Identify the preparation type.
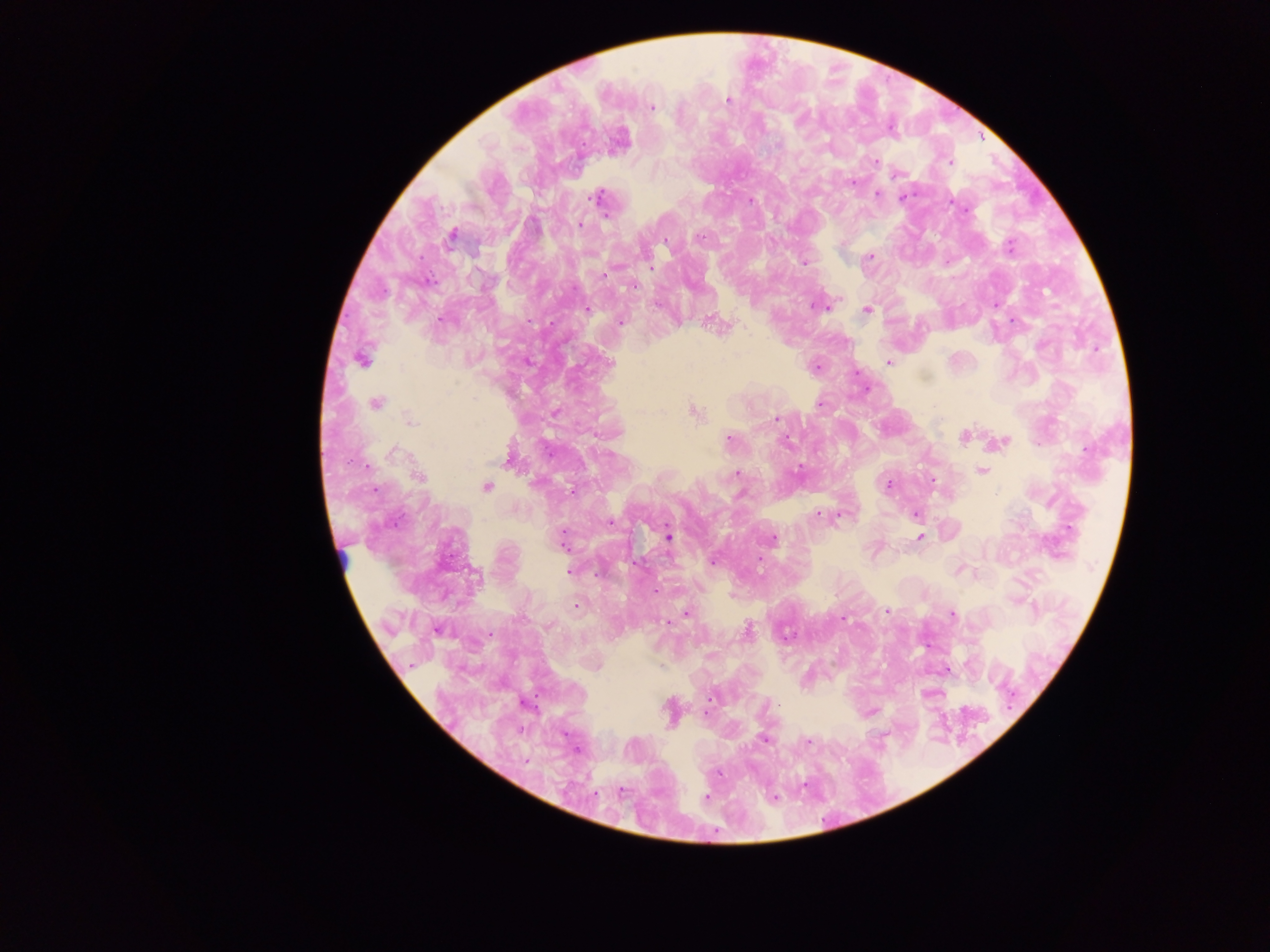
This is a thick smear.

Approximate centers as [x, y] in pixels. Plasmodium parasite locations: [727, 100], [651, 107], [875, 162], [949, 162], [853, 181], [877, 195], [598, 197], [903, 197], [750, 200], [581, 223], [451, 235], [699, 237], [1009, 246], [869, 257], [803, 262], [650, 267], [604, 275], [995, 304], [824, 306], [868, 309], [587, 310], [619, 321], [1014, 321], [711, 323], [361, 359], [888, 362], [816, 367], [866, 388], [376, 403], [820, 403], [693, 411], [554, 412], [776, 418], [409, 421], [964, 436], [728, 439], [785, 441], [1002, 442], [392, 451], [982, 470], [736, 473], [418, 476], [932, 480], [888, 484], [485, 487], [573, 490], [819, 513], [916, 513], [838, 514], [668, 536], [921, 536], [563, 539], [770, 539], [959, 569], [569, 572], [655, 590], [576, 604], [887, 611], [687, 614], [952, 614], [842, 618], [667, 622], [746, 630], [947, 670], [711, 697], [669, 712], [705, 712], [869, 713], [764, 738], [807, 740], [773, 796], [706, 798]. Sample from Ghana. Photographed through a microscope with a mobile-phone camera. Image is 1270×952 pixels. One field of view.